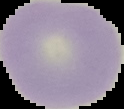
preparation = thin blood smear
malaria status = uninfected
image size = 124×109 pixels
image type = segmented cell region on a black background